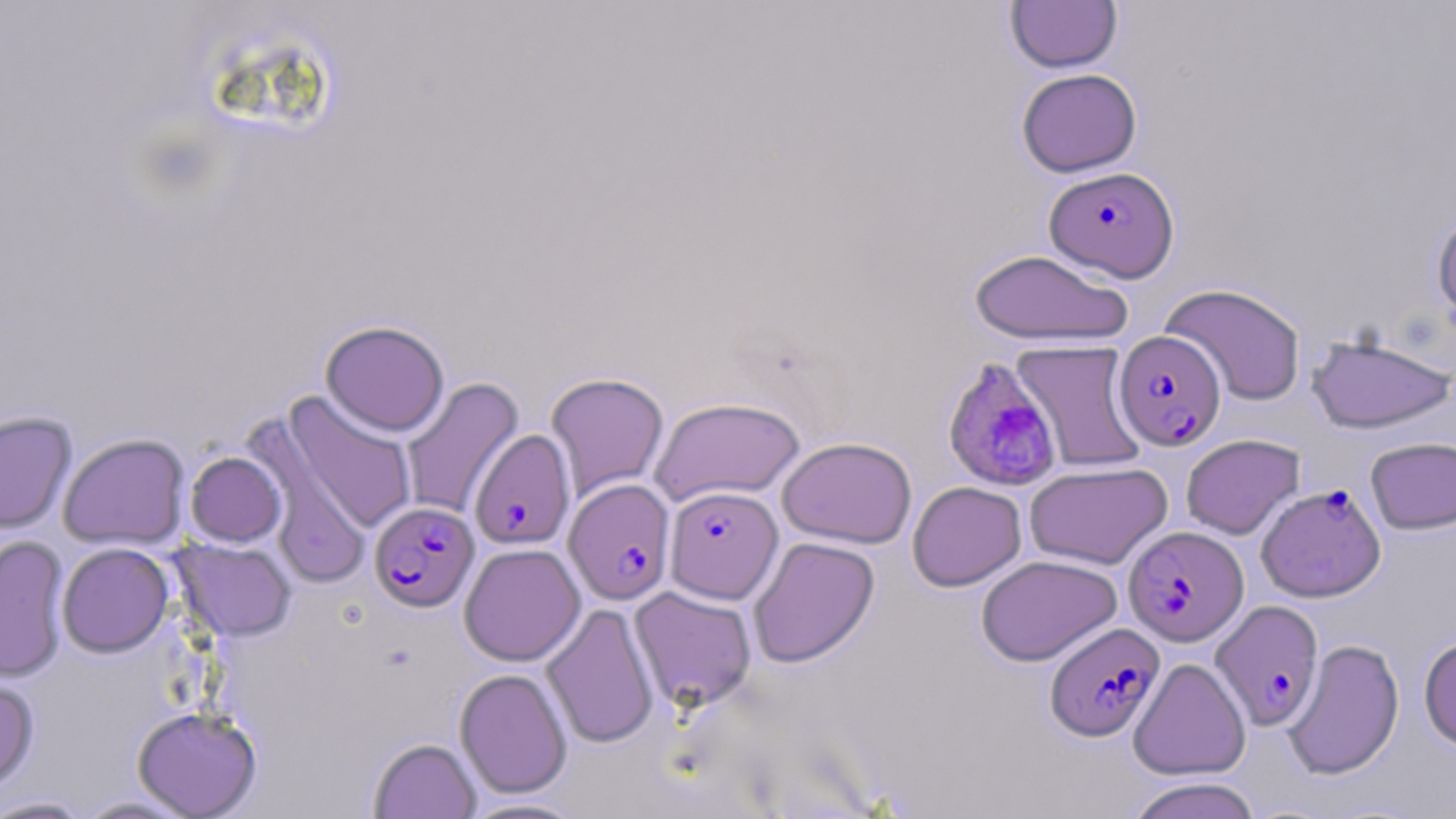

{
  "plasmodium_falciparum_infected_red_blood_cell_locations": "approximate bounding boxes as (x1, y1, x2, y2) in pixels: (1044, 166, 1179, 282), (1114, 330, 1226, 450), (941, 358, 1064, 494), (469, 428, 576, 551), (564, 478, 676, 605), (1256, 483, 1386, 602), (665, 485, 783, 604), (369, 501, 479, 612), (1123, 526, 1248, 646), (1210, 600, 1324, 731), (1044, 621, 1164, 741)",
  "slide_level_diagnosis": "Plasmodium falciparum",
  "image_size": "1456×819 pixels",
  "uninfected_red_blood_cell_locations": "approximate bounding boxes as (x1, y1, x2, y2) in pixels: (1006, 0, 1122, 73), (1016, 68, 1142, 177), (1431, 209, 1456, 332), (968, 248, 1134, 347), (1160, 283, 1307, 405), (320, 320, 450, 437), (1306, 333, 1455, 434), (1010, 340, 1148, 472), (545, 372, 670, 501), (400, 377, 524, 520), (283, 392, 418, 535), (649, 396, 806, 506), (0, 410, 77, 533), (58, 433, 190, 550), (1180, 434, 1305, 539), (777, 436, 917, 548), (1365, 436, 1456, 535), (254, 441, 373, 593), (185, 451, 286, 546), (1024, 461, 1173, 570), (907, 481, 1027, 591), (0, 534, 70, 682), (748, 536, 880, 667), (173, 538, 297, 642), (57, 542, 174, 657), (459, 542, 586, 666), (976, 554, 1122, 666), (629, 585, 757, 712), (541, 602, 660, 750), (1419, 633, 1456, 751), (1283, 638, 1404, 780), (1127, 657, 1251, 781), (455, 668, 573, 799), (0, 677, 40, 794), (132, 705, 263, 818), (368, 737, 481, 818), (1124, 777, 1264, 819), (0, 795, 93, 818), (73, 795, 199, 818), (457, 796, 590, 818)",
  "field_of_view": "one of a larger specimen",
  "magnification": "1000x",
  "modality": "light microscopy",
  "preparation": "thin blood smear",
  "stain": "May-Grünwald-Giemsa"
}